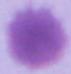
magnification: 1000x
identification: red blood cell
modality: photomicrograph